Locate and identify every blood parasite.
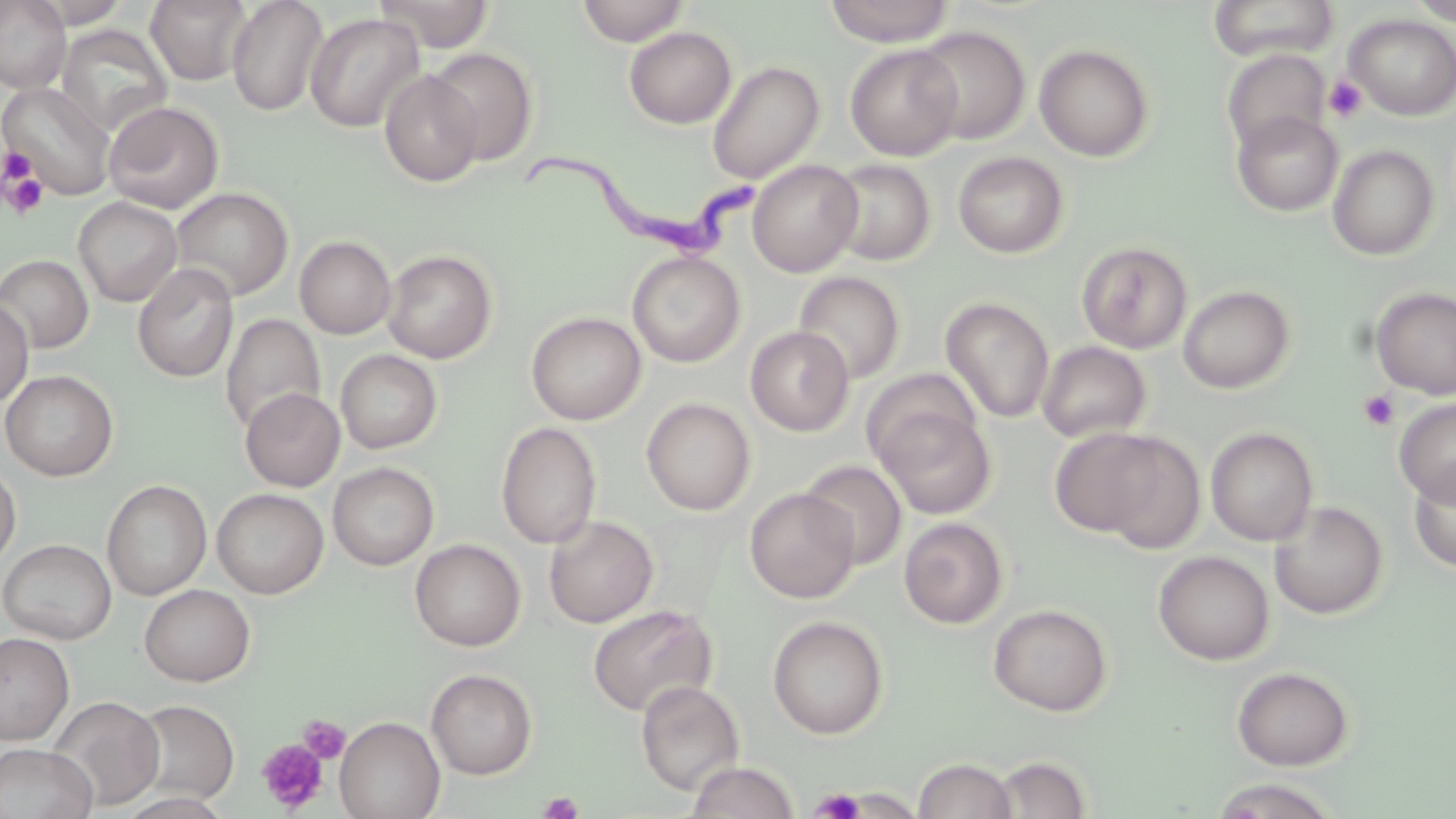
Approximate bounding boxes as [x1, y1, x2, y2] in pixels.
Trypanosoma brucei: [509, 144, 771, 255].
No Plasmodium falciparum, Plasmodium ovale, Plasmodium malariae, Plasmodium vivax, or Babesia divergens observed.

{
  "slide_level_diagnosis": "Trypanosoma brucei",
  "preparation": "thin blood film",
  "modality": "light microscopy",
  "magnification": "1000x",
  "field_of_view": "one of a larger specimen",
  "stain": "May-Grünwald-Giemsa",
  "uninfected_red_blood_cell_locations": "approximate bounding boxes as [x1, y1, x2, y2] in pixels: [0, 0, 72, 93], [22, 0, 132, 28], [145, 0, 252, 86], [226, 0, 329, 117], [375, 0, 496, 53], [576, 0, 690, 46], [824, 0, 953, 46], [1206, 0, 1340, 62], [1407, 0, 1456, 25], [305, 12, 424, 133], [1343, 14, 1456, 120], [55, 23, 173, 136], [912, 25, 1031, 144], [624, 27, 736, 129], [845, 44, 963, 161], [1034, 44, 1155, 162], [426, 47, 539, 166], [1222, 49, 1330, 155], [707, 61, 825, 184], [379, 69, 484, 187], [1, 82, 115, 200], [104, 101, 224, 213], [1232, 110, 1343, 216], [1327, 144, 1440, 261], [953, 152, 1069, 258], [828, 158, 935, 267], [747, 160, 864, 277], [169, 187, 293, 302], [73, 197, 182, 307], [294, 236, 395, 339], [1076, 241, 1192, 354], [381, 249, 497, 363], [627, 251, 745, 368], [0, 254, 94, 354], [132, 263, 239, 383], [792, 271, 905, 384], [1177, 285, 1295, 394], [1370, 287, 1456, 400], [941, 296, 1055, 423], [0, 297, 34, 408], [526, 312, 647, 425], [220, 314, 325, 435], [745, 326, 854, 436], [1036, 341, 1151, 443], [335, 349, 442, 454], [862, 368, 982, 469], [0, 370, 118, 481], [240, 387, 345, 491], [1394, 397, 1456, 505], [641, 398, 755, 515], [875, 406, 996, 519], [495, 422, 602, 549], [1048, 427, 1171, 537], [1205, 427, 1318, 546], [1092, 431, 1207, 551], [799, 459, 907, 569], [0, 461, 21, 572], [328, 462, 439, 570], [1408, 463, 1456, 572], [101, 479, 212, 600], [212, 488, 328, 598], [744, 488, 860, 603], [1269, 500, 1388, 619], [544, 515, 658, 628], [899, 517, 1009, 629], [1, 539, 116, 645], [410, 539, 526, 651], [1153, 550, 1275, 665], [139, 584, 255, 686], [587, 604, 717, 718], [988, 604, 1113, 716], [767, 615, 889, 740], [0, 632, 74, 744], [1231, 666, 1354, 771], [426, 668, 538, 779], [636, 680, 744, 796], [47, 696, 165, 811], [130, 699, 240, 805], [334, 716, 445, 819], [0, 743, 97, 819], [991, 755, 1093, 818], [913, 757, 1018, 819], [686, 761, 800, 819], [1208, 778, 1340, 818]",
  "image_size": "1456×819 pixels",
  "platelet_locations": "approximate bounding boxes as [x1, y1, x2, y2] in pixels: [1324, 75, 1368, 122], [2, 149, 36, 187], [3, 170, 48, 219], [1359, 390, 1400, 431], [298, 714, 350, 763], [257, 739, 329, 812], [810, 788, 865, 819], [538, 791, 584, 819]"
}